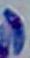
Summary:
  - Magnification: 1000x
  - Identification: Toxoplasma gondii
  - Modality: micrograph